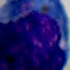

magnification = 1000x
identification = white blood cell
modality = photomicrograph